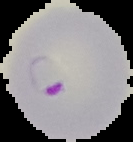

Malaria status: parasitized. Image is 133×142 pixels. From a thin blood film. Segmented cell region on a black background.